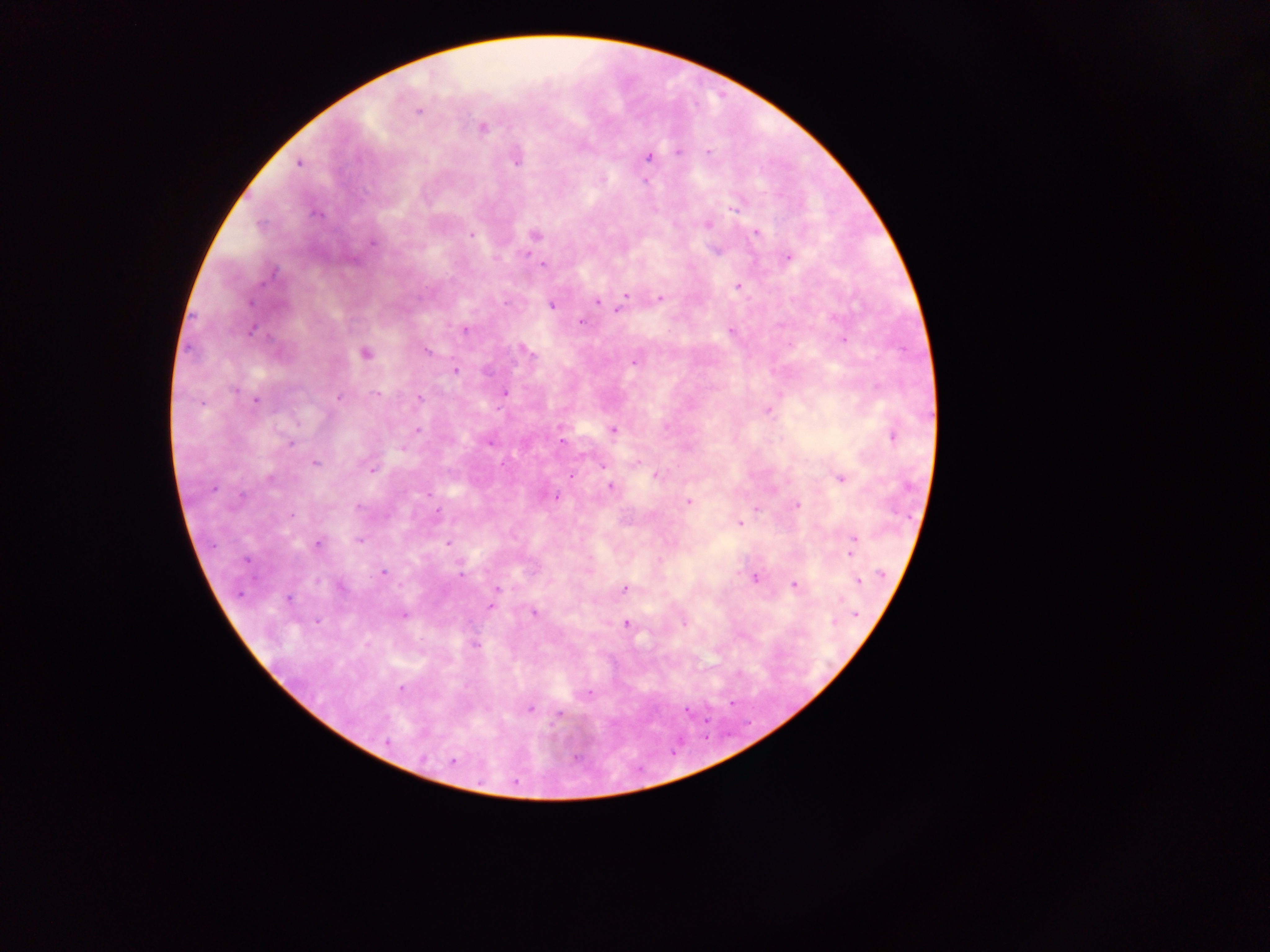
capture = mobile-phone photograph through a microscope
Plasmodium parasite locations = approximate centers as [x, y] in pixels: [418, 111], [482, 128], [678, 151], [708, 152], [648, 157], [516, 161], [299, 163], [645, 180], [733, 209], [317, 214], [708, 224], [260, 225], [756, 233], [471, 235], [535, 235], [372, 242], [788, 257], [542, 264], [737, 286], [626, 295], [660, 298], [597, 301], [251, 303], [552, 305], [619, 309], [581, 322], [252, 330], [465, 330], [730, 330], [843, 340], [427, 350], [527, 352], [364, 354], [634, 362], [455, 371], [235, 390], [505, 392], [377, 394], [339, 397], [420, 398], [257, 401], [767, 411], [418, 430], [612, 430], [893, 436], [561, 441], [291, 444], [489, 444], [401, 448], [316, 462], [602, 465], [371, 469], [656, 475], [571, 476], [271, 478], [840, 479], [610, 486], [212, 490], [428, 494], [556, 498], [688, 502], [797, 505], [359, 507], [758, 510], [438, 511], [291, 516], [740, 523], [854, 539], [359, 541], [447, 543], [317, 544], [851, 552], [247, 560], [383, 572], [880, 573], [460, 575], [755, 579], [858, 581], [794, 584], [341, 588], [497, 588], [624, 588], [288, 599], [841, 599], [493, 600], [491, 606], [534, 612], [856, 614], [404, 615], [317, 621], [684, 622], [834, 622], [626, 623], [475, 645], [401, 689], [587, 693], [530, 709], [559, 715], [388, 743], [453, 762]
country = Ghana
field of view = single
preparation = thick blood film
image size = 1270×952 pixels